Describe the morphology of the erythrocytes.
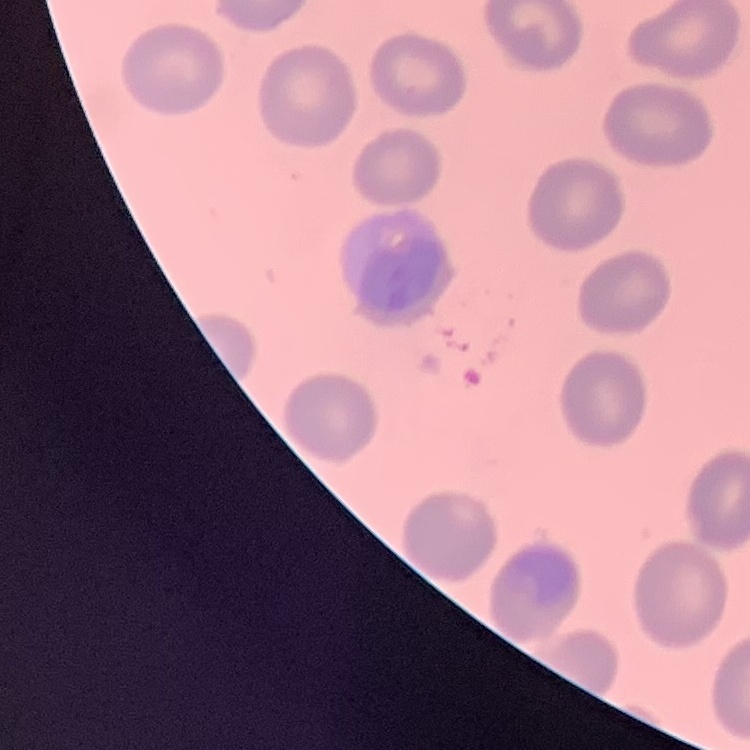
They show no rouleaux formation.

Summary:
  - Stain: Field's or Giemsa
  - Preparation: thin blood smear
  - Image type: one tile cut from a larger photomicrograph